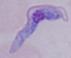

Summary:
  - Modality: photomicrograph
  - Identification: trypanosome
  - Magnification: 1000x